Describe the morphology of the erythrocytes.
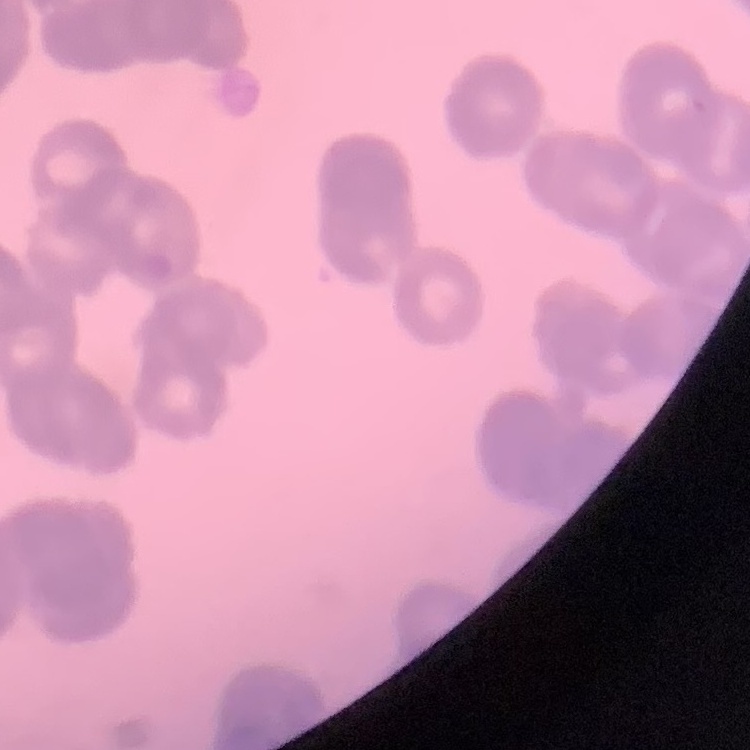

They show rouleaux formation.

Thin peripheral smear. One tile cut from a larger photomicrograph. Field's or Giemsa stain.